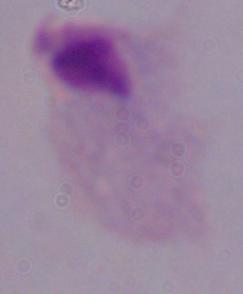
Summary:
  - Magnification: 1000x
  - Modality: micrograph
  - Identification: trichomonad